Evaluate for malaria.
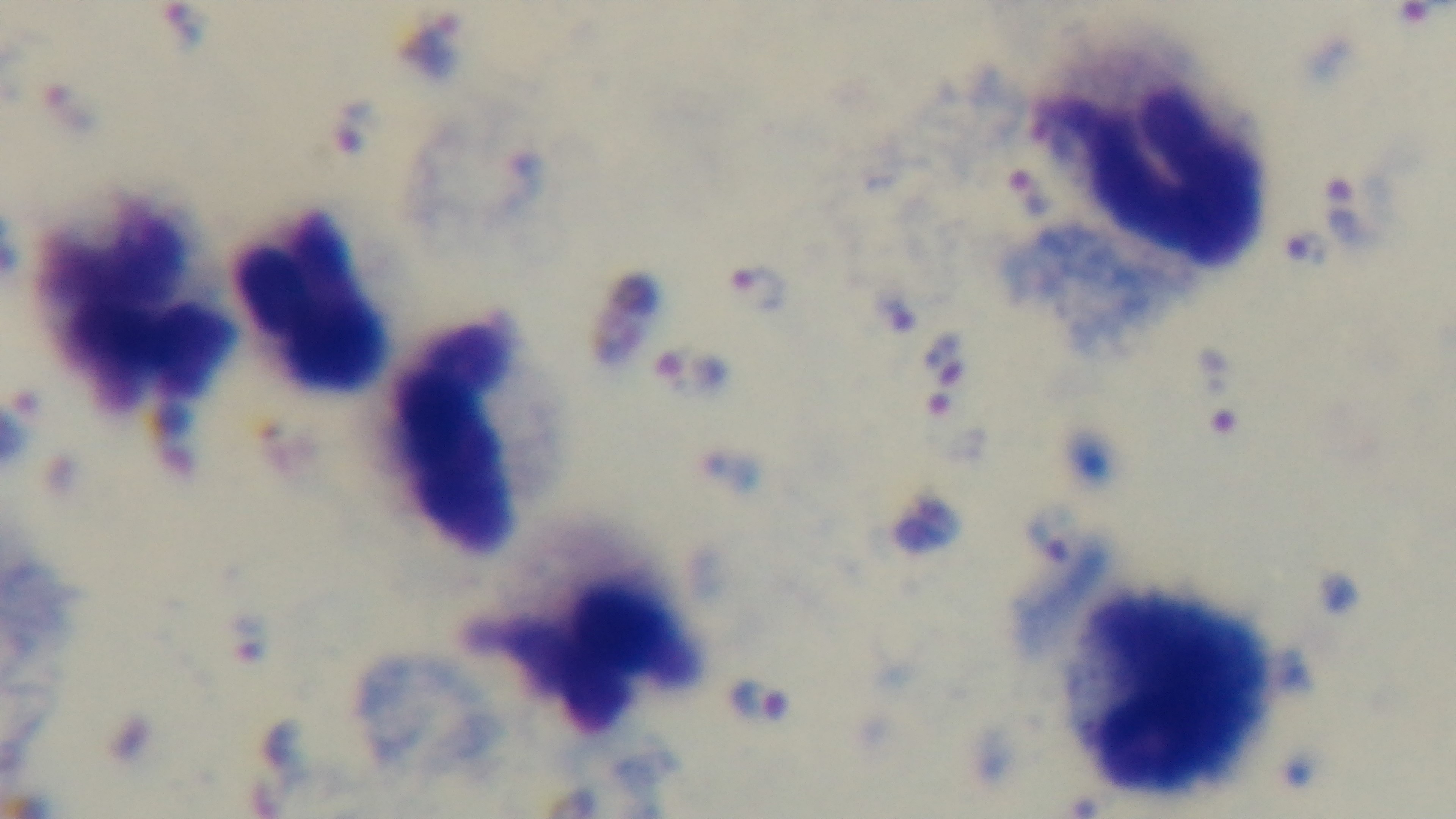
It is infected.

{
  "stain": "Giemsa",
  "preparation": "thick",
  "field_of_view": "single",
  "objective": "100x oil immersion",
  "modality": "light microscopy",
  "capture": "mounted 4K digital camera"
}